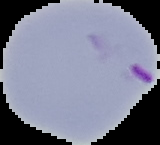

Summary:
  - Result: malaria parasites identified
  - Image size: 160×145 pixels
  - Image type: segmented cell region with the area outside set to black
  - Preparation: thin blood smear